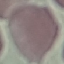 Result: no malaria parasites seen. Giemsa stain. Thin smear of blood. Cell patch, automatically extracted from a larger field of view and resized to 64 × 64 pixels. Photographed with a smartphone camera at the microscope eyepiece.